Point out each leukocyte.
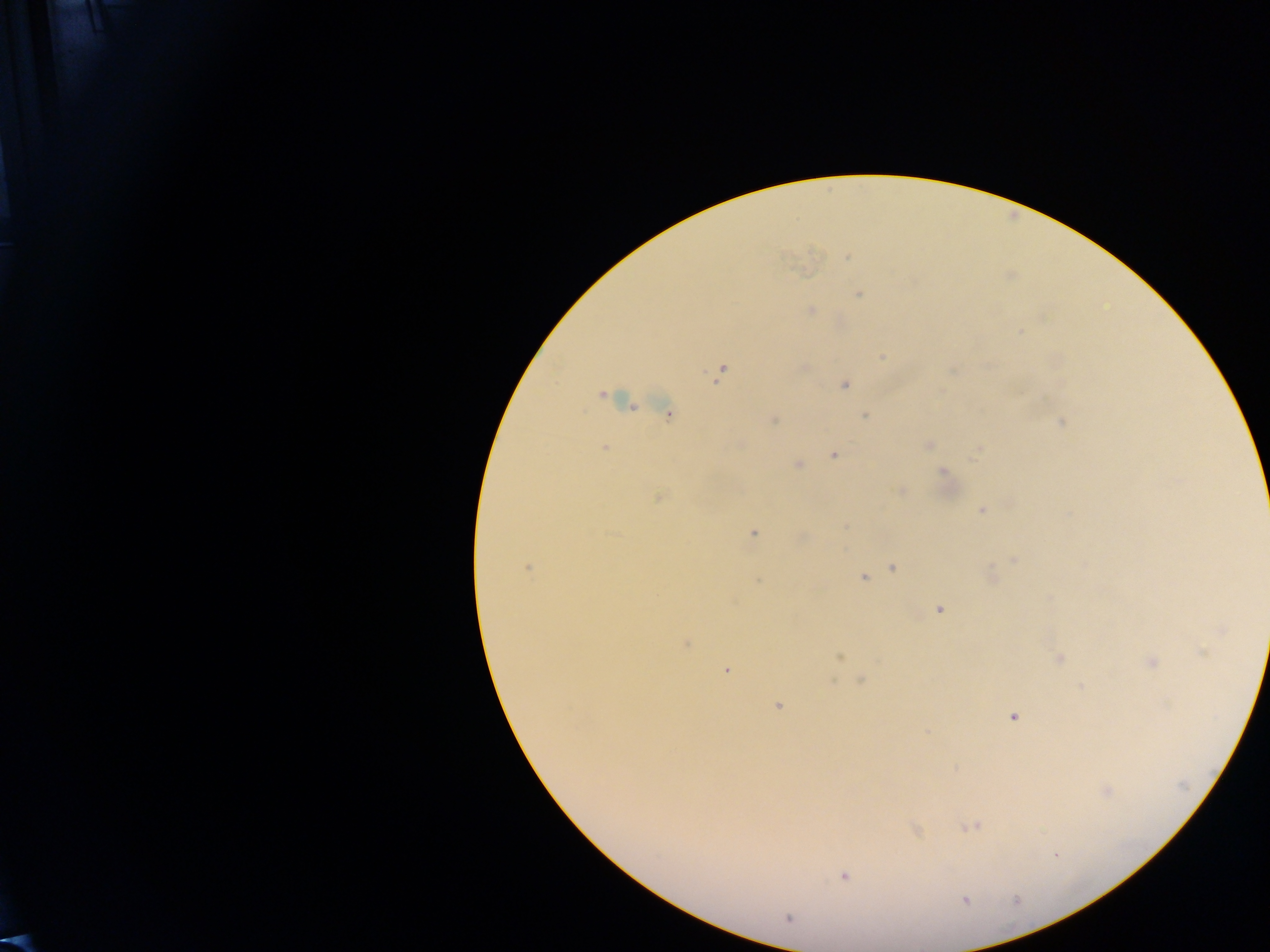
No leukocytes observed.

{
  "field_of_view": "single",
  "plasmodium_parasite_locations": "approximate centers as {x, y} in pixels: {847, 256}, {858, 294}, {810, 311}, {1019, 331}, {883, 357}, {721, 372}, {844, 385}, {601, 394}, {630, 404}, {669, 415}, {866, 416}, {773, 420}, {1060, 421}, {928, 445}, {604, 447}, {978, 450}, {834, 455}, {797, 465}, {944, 474}, {900, 490}, {659, 496}, {981, 510}, {846, 526}, {753, 533}, {801, 537}, {1014, 559}, {527, 567}, {893, 567}, {992, 575}, {863, 577}, {757, 580}, {939, 608}, {685, 643}, {1202, 652}, {837, 657}, {1058, 659}, {1151, 662}, {725, 669}, {861, 680}, {1082, 686}, {777, 705}, {1012, 716}, {926, 732}, {1105, 791}, {971, 826}, {916, 830}, {843, 876}, {788, 918}",
  "preparation": "thick blood smear",
  "image_size": "1270×952 pixels",
  "capture": "mobile-phone photograph through a microscope",
  "country": "Ghana"
}